Comment on the morphology of the erythrocytes.
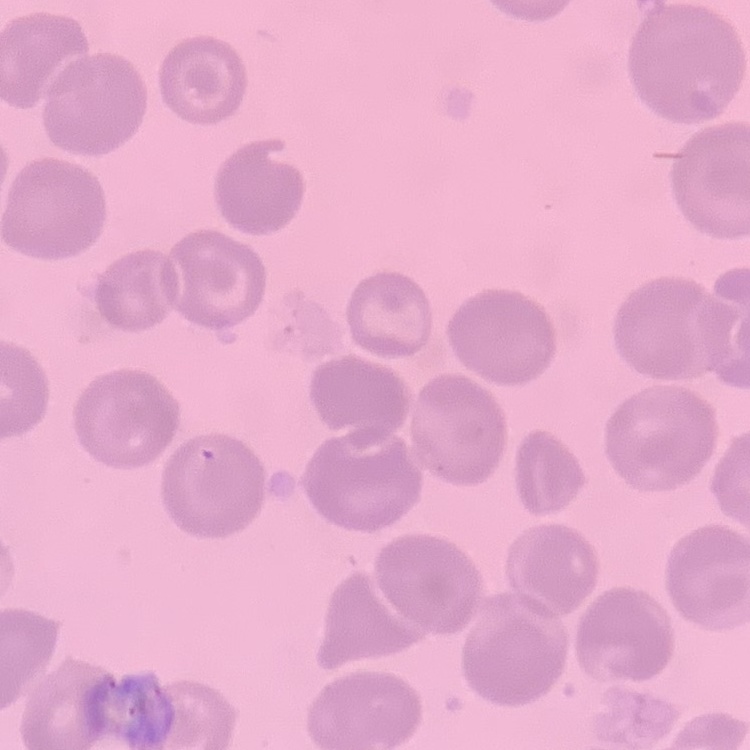
No rouleaux formation.

preparation: thin peripheral smear
stain: Field's or Giemsa
image_type: square crop of a larger photomicrograph